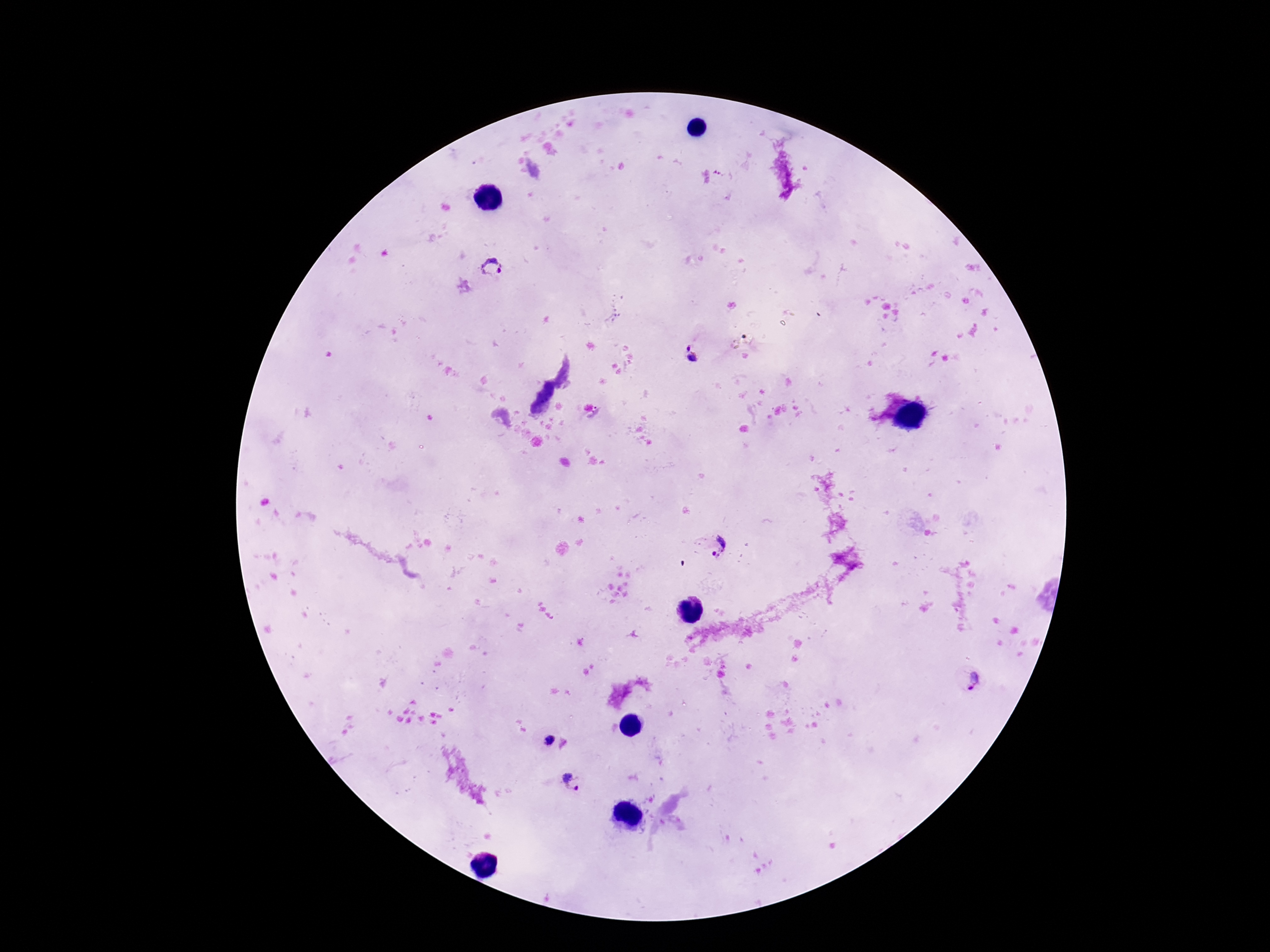
Approximate centers as (x, y) in pixels. Plasmodium parasite locations: (492, 265), (692, 358), (717, 545), (973, 681), (547, 742), (579, 783). Patient malaria status: infected. One field from this slide. 100x magnification. Smartphone photograph taken through the microscope eyepiece. Giemsa-stained preparation. Image is 1270×952 pixels. Thick blood smear.